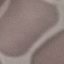
result = negative for malaria parasites
capture = smartphone camera at the microscope eyepiece
stain = Giemsa
image type = cell patch, automatically extracted from a larger field of view and resized to 64 × 64 pixels
preparation = thin blood film